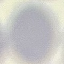

Result: no malaria parasites detected. Giemsa stain. Thin blood smear. Cell patch, automatically extracted from a larger field of view and resized to 64 × 64 pixels. Photographed with a smartphone camera at the microscope eyepiece.